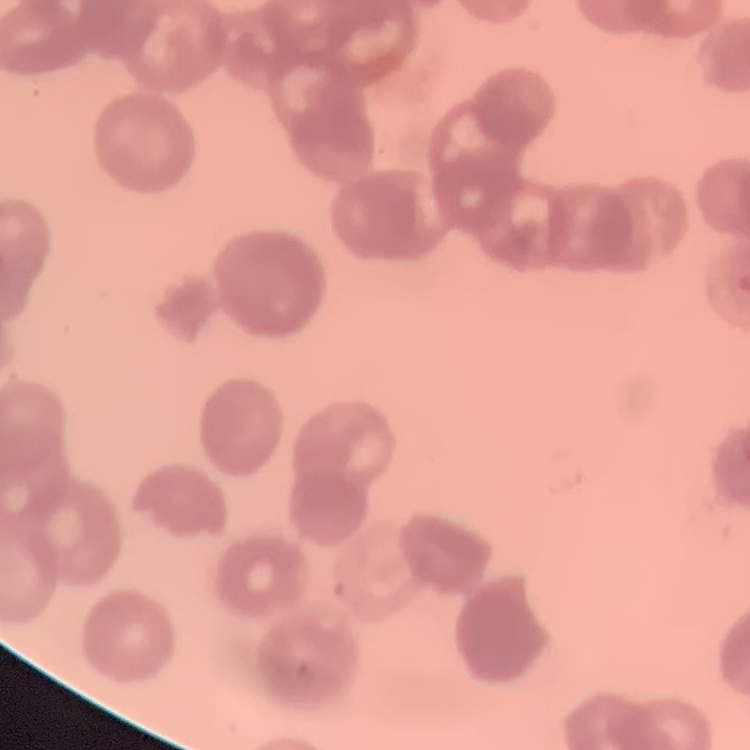
The erythrocytes exhibit rouleaux formation. Square crop of a larger photomicrograph. Thin blood film. Stained with either Field's or Giemsa.